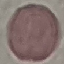

malaria status = uninfected
capture = smartphone through the microscope eyepiece
image type = cell patch, automatically extracted from a larger field of view and resized to 64 × 64 pixels
stain = Giemsa
preparation = thin blood film